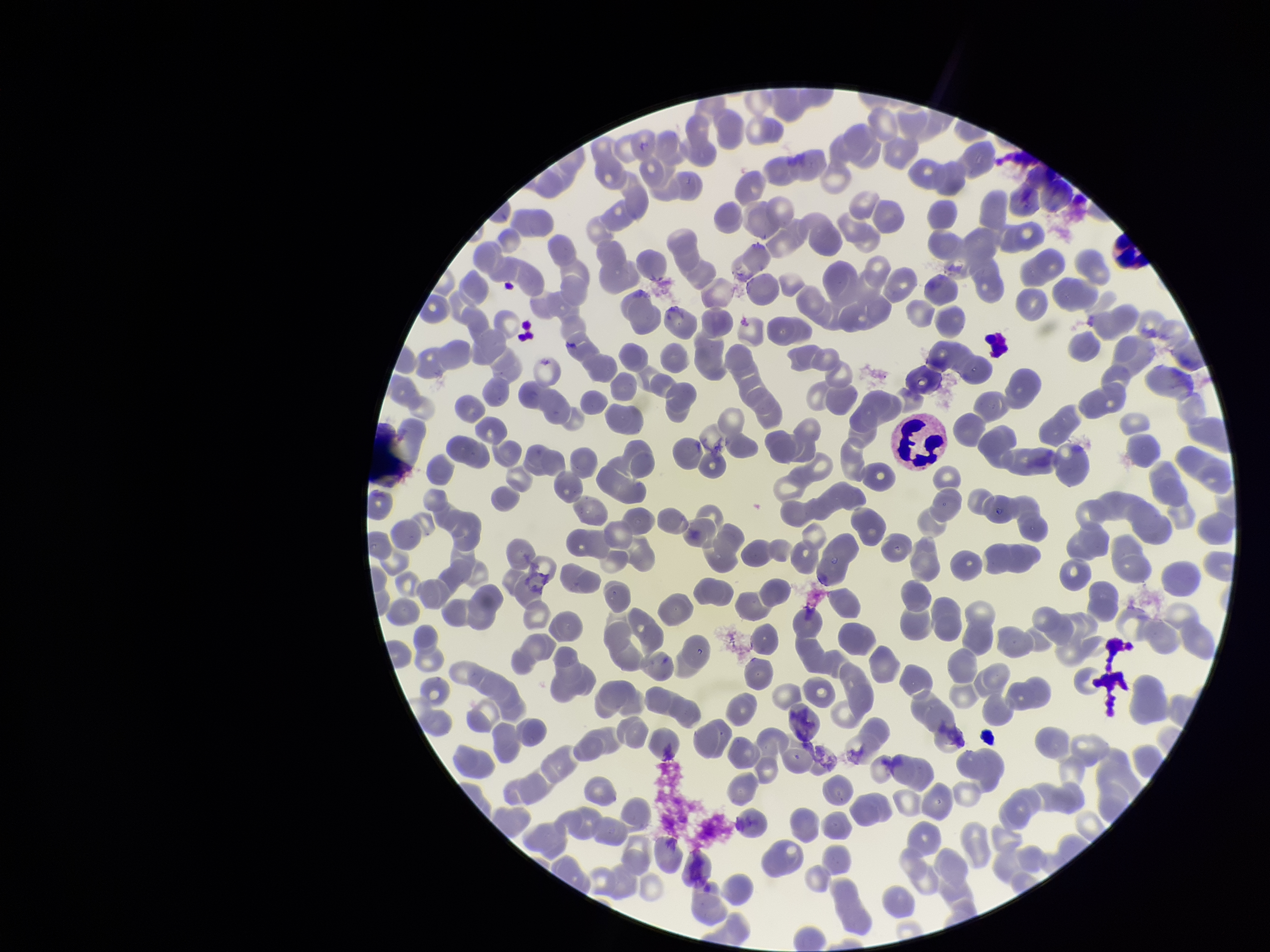

Summary:
  - Parasitized red blood cells: none identified
  - Preparation: thin
  - Parasitized red blood cell count: 0
  - Patient malaria status: negative
  - Red blood cell count: 275
  - Stain: Giemsa
  - Image size: 1270×952 pixels
  - Field of view: single
  - Capture: smartphone photograph through the microscope eyepiece